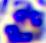

modality = micrograph
identification = white blood cell
magnification = 400x